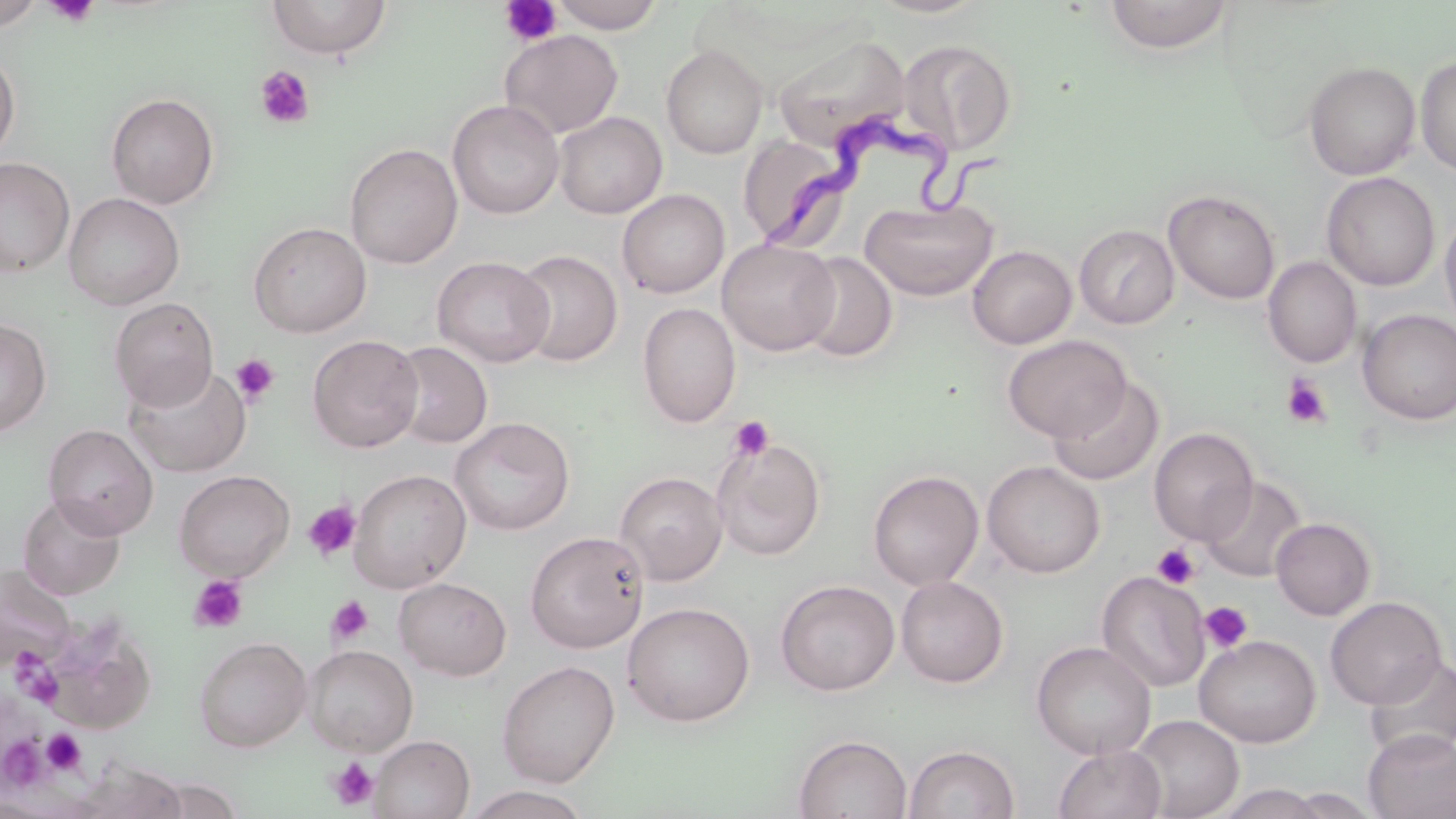 Approximate bounding boxes as (x1,y1)-(x2,y2) corner pairs in pixels. Uninfected red blood cell locations: (0,0)-(45,30), (267,0)-(392,59), (549,0)-(667,33), (869,0)-(990,19), (1104,0)-(1234,54), (499,29)-(623,139), (773,35)-(912,153), (898,39)-(1016,155), (661,45)-(768,159), (0,50)-(20,162), (1415,54)-(1456,176), (1304,61)-(1421,180), (105,92)-(219,209), (447,99)-(564,219), (553,111)-(667,218), (738,134)-(850,249), (344,143)-(463,269), (0,156)-(75,277), (1321,172)-(1440,291), (617,189)-(729,298), (1164,190)-(1280,304), (64,192)-(184,309), (859,198)-(998,300), (1440,209)-(1456,338), (248,221)-(371,337), (1074,224)-(1179,329), (717,239)-(840,356), (967,245)-(1076,348), (511,249)-(623,367), (795,251)-(897,362), (1262,255)-(1362,368), (432,256)-(555,367), (110,297)-(219,411), (637,302)-(740,428), (1358,309)-(1456,425), (0,317)-(52,436), (307,334)-(424,453), (1003,335)-(1131,442), (389,341)-(492,448), (125,364)-(251,476), (1047,376)-(1164,487), (449,417)-(575,535), (43,424)-(158,539), (1149,427)-(1259,546), (712,437)-(826,560), (982,460)-(1105,578), (349,468)-(471,592), (173,469)-(295,581), (867,469)-(984,590), (614,471)-(727,585), (1200,476)-(1307,583), (17,493)-(126,601), (1270,517)-(1376,620), (525,530)-(649,653), (0,564)-(73,669), (1096,570)-(1210,692), (896,575)-(1008,688), (394,577)-(512,680), (775,580)-(899,696), (1325,596)-(1448,709), (622,602)-(755,727), (1194,634)-(1321,747), (194,636)-(312,752), (1031,641)-(1156,759), (302,644)-(418,756), (1363,656)-(1456,762), (497,659)-(620,787), (1129,715)-(1244,818), (1363,729)-(1456,819), (793,733)-(912,819), (369,734)-(475,819), (903,744)-(1020,819), (1052,744)-(1167,819), (72,761)-(189,819), (145,776)-(243,818), (1215,784)-(1330,819), (462,785)-(594,819), (1277,788)-(1384,818). Platelet locations: (45,0)-(100,28), (500,1)-(563,47), (254,65)-(315,129), (231,353)-(281,406), (1281,375)-(1331,428), (729,416)-(775,462), (301,500)-(361,562), (1152,543)-(1200,589), (188,575)-(249,633), (327,595)-(373,645), (1199,601)-(1254,654), (9,649)-(54,689), (26,667)-(62,707), (41,729)-(86,776), (1,735)-(49,791), (327,755)-(380,811). Trypanosoma brucei locations: (760,120)-(1012,259). Slide-level diagnosis: Trypanosoma brucei. 1000x magnification. Image is 1456×819 pixels. Single field of view. Light microscopy. Thin blood film. May-Grünwald-Giemsa stain.